Classify this cell by malaria status.
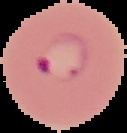

It is parasitized.

Summary:
  - Image type: segmented cell region with the area outside set to black
  - Image size: 127×133 pixels
  - Preparation: thin blood film